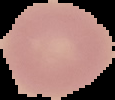
Summary:
  - Image type: cell region segmented out of the field of view; surrounding area masked to black
  - Image size: 115×100 pixels
  - Result: no Plasmodium parasites detected
  - Preparation: thin blood smear